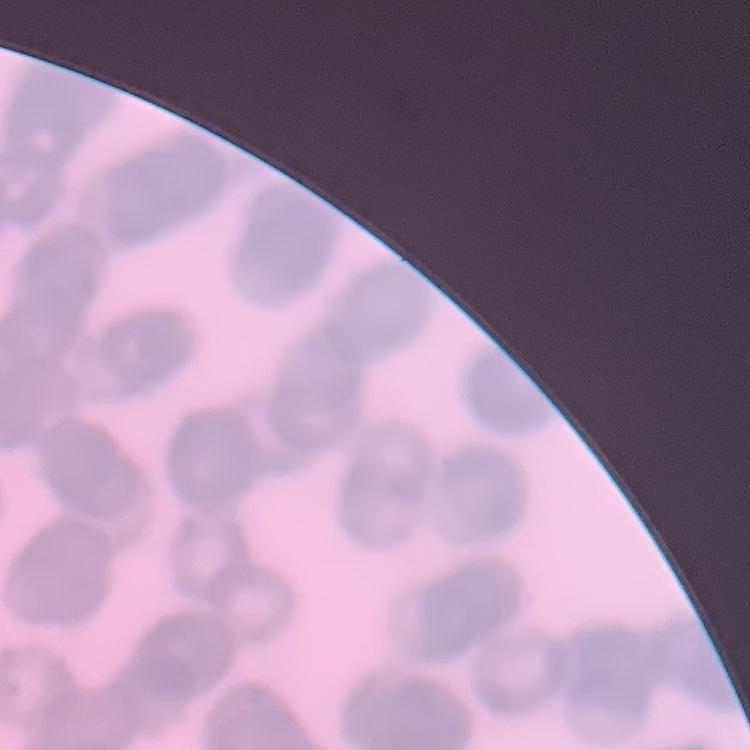
erythrocyte morphology = rouleaux formation
preparation = thin blood smear
image type = square crop of a larger photomicrograph
stain = Field's or Giemsa